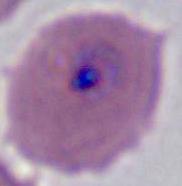

Summary:
  - Modality: photomicrograph
  - Identification: Plasmodium
  - Magnification: 400x or 1000x